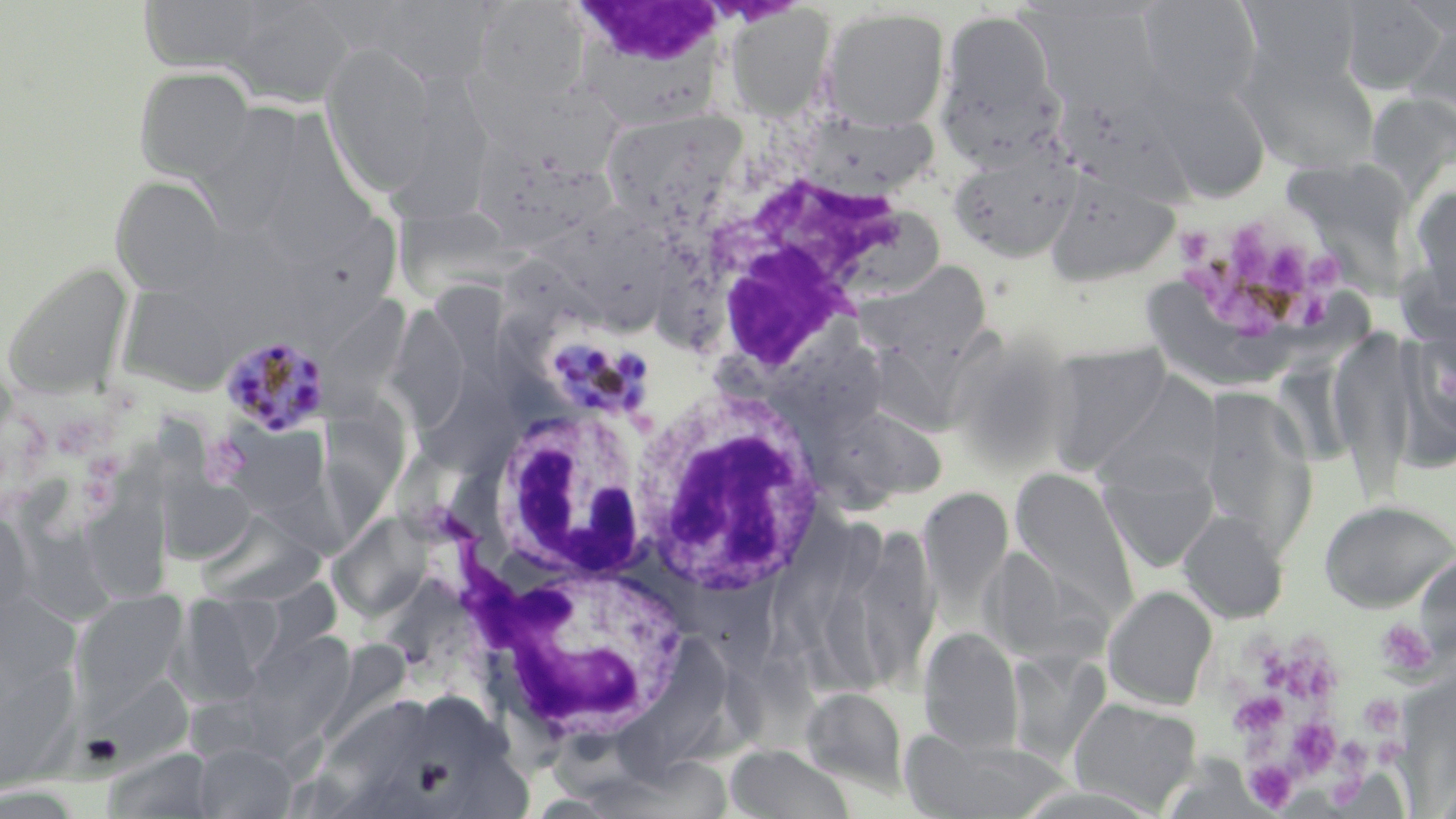 Approximate bounding boxes as [x1, y1, x2, y2] in pixels. Platelet locations: [1174, 212, 1356, 347], [1375, 618, 1437, 679], [1277, 648, 1340, 705], [1229, 691, 1288, 737], [1359, 693, 1405, 734], [1287, 719, 1341, 772], [1371, 737, 1406, 764], [1246, 762, 1298, 809]. Plasmodium malariae-infected red blood cell locations: [529, 324, 660, 426], [219, 331, 330, 436]. Uninfected red blood cell locations: [137, 0, 278, 74], [1137, 0, 1262, 107], [1238, 0, 1364, 90], [1335, 0, 1448, 94], [225, 1, 355, 107], [469, 1, 590, 105], [568, 1, 728, 120], [358, 3, 498, 84], [723, 4, 835, 120], [820, 6, 950, 131], [935, 8, 1065, 164], [1405, 17, 1456, 129], [320, 41, 439, 197], [1244, 56, 1380, 173], [134, 66, 256, 180], [1149, 75, 1271, 202], [1367, 91, 1456, 197], [387, 92, 487, 226], [194, 94, 306, 226], [598, 106, 748, 227], [802, 113, 939, 198], [475, 133, 623, 253], [948, 144, 1081, 262], [1284, 153, 1424, 302], [1044, 171, 1180, 287], [110, 175, 228, 296], [1405, 180, 1456, 314], [389, 200, 497, 297], [547, 202, 680, 338], [275, 215, 395, 342], [2, 259, 134, 397], [862, 262, 993, 364], [114, 272, 262, 394], [1130, 274, 1290, 395], [391, 302, 465, 442], [775, 325, 890, 434], [871, 326, 1014, 427], [1328, 328, 1419, 499], [1400, 331, 1456, 466], [1043, 343, 1173, 473], [1093, 375, 1222, 496], [1199, 386, 1318, 555], [319, 396, 412, 537], [826, 401, 944, 503], [1098, 453, 1219, 572], [96, 456, 170, 601], [17, 464, 115, 631], [155, 465, 259, 565], [1010, 468, 1137, 614], [918, 487, 1013, 616], [1319, 499, 1456, 612], [0, 503, 35, 621], [324, 505, 438, 628], [197, 509, 327, 606], [1178, 509, 1288, 623], [857, 519, 955, 694], [1103, 585, 1217, 709], [70, 590, 189, 712], [0, 592, 82, 694], [171, 592, 283, 706], [919, 626, 1025, 754], [244, 632, 358, 751], [622, 639, 732, 777], [0, 642, 83, 795], [1005, 649, 1110, 765], [83, 672, 196, 767], [801, 687, 909, 795], [308, 691, 436, 813], [1068, 698, 1201, 812], [899, 729, 1070, 818], [190, 742, 297, 818], [725, 744, 857, 819]. White blood cell locations: [562, 0, 733, 112], [683, 126, 945, 364], [629, 383, 829, 601], [483, 404, 651, 590], [493, 555, 694, 748]. Slide-level diagnosis: Plasmodium malariae. Light microscopy. Captured at 1000x magnification. May-Grünwald-Giemsa stain. Image is 1456×819 pixels. One field of a larger specimen. Thin blood film.